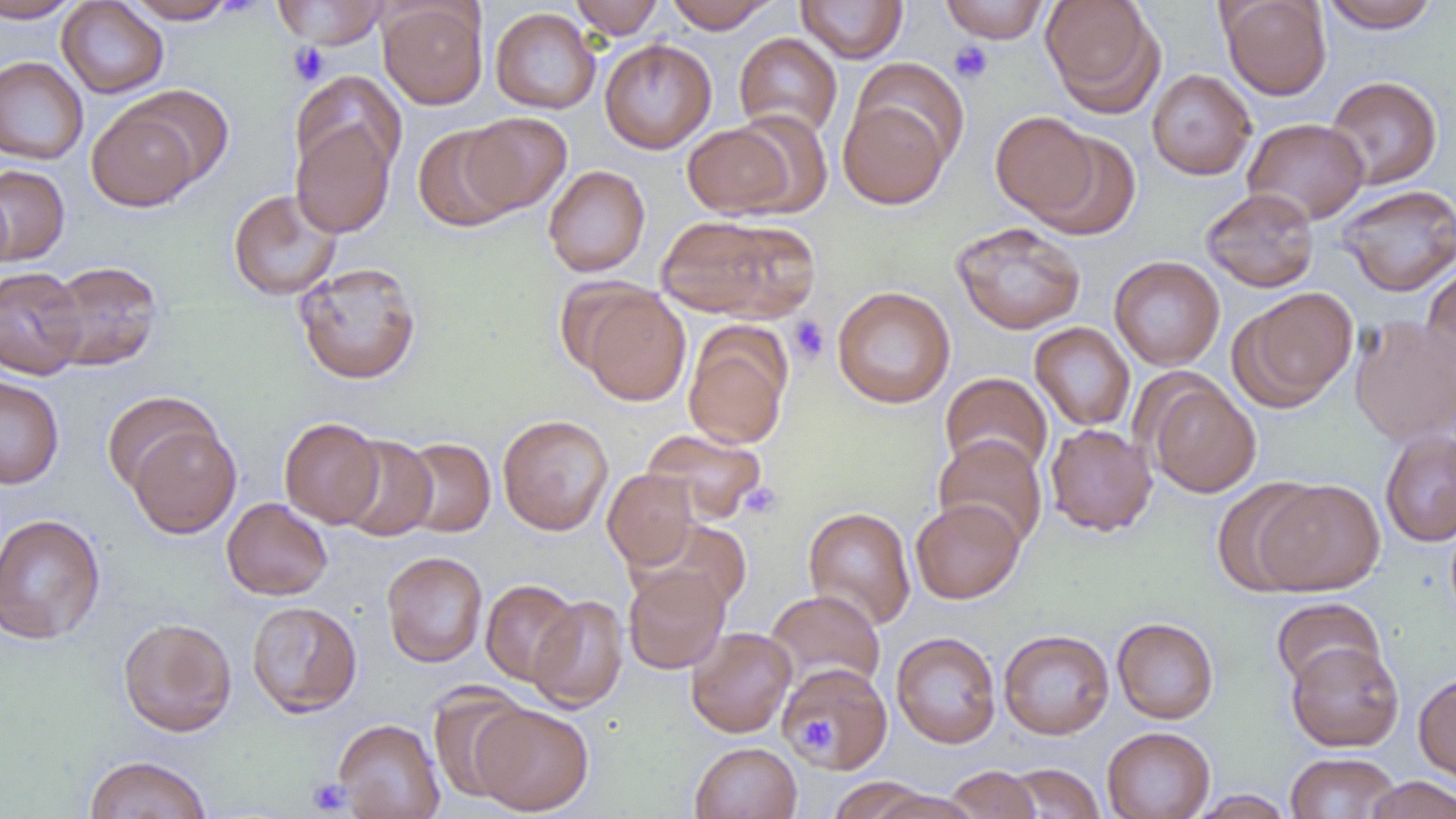

Summary:
  - Coordinate format: approximate bounding boxes as (x1,y1)-(x2,y2) corner pairs in pixels
  - Platelet locations: (948,41)-(993,84), (287,43)-(329,85), (788,316)-(830,365), (738,482)-(783,521), (798,716)-(835,751), (306,777)-(352,815)
  - Uninfected red blood cell locations: (0,0)-(83,23), (121,0)-(238,24), (272,0)-(389,48), (569,0)-(665,38), (664,0)-(776,33), (796,0)-(908,63), (939,0)-(1050,43), (1041,0)-(1164,115), (1219,0)-(1332,100), (1319,0)-(1442,33), (57,1)-(169,99), (379,2)-(488,109), (489,7)-(600,114), (734,32)-(843,139), (599,39)-(716,154), (0,56)-(89,164), (1146,69)-(1257,180), (290,71)-(406,181), (1324,75)-(1443,189), (121,84)-(235,188), (838,95)-(953,209), (86,103)-(201,212), (727,110)-(835,216), (991,111)-(1099,222), (461,112)-(572,215), (1242,117)-(1370,224), (290,120)-(396,239), (681,121)-(802,219), (413,123)-(523,232), (1030,131)-(1140,241), (0,164)-(69,266), (544,165)-(650,276), (1337,184)-(1456,296), (1201,187)-(1320,292), (228,189)-(343,301), (655,214)-(806,319), (950,221)-(1086,335), (1109,255)-(1225,371), (44,260)-(163,371), (293,261)-(422,385), (1422,263)-(1456,384), (0,265)-(87,379), (572,284)-(691,405), (832,286)-(956,409), (1232,287)-(1358,411), (1349,315)-(1456,445), (1029,322)-(1136,432), (683,324)-(793,450), (940,372)-(1053,478), (0,375)-(65,489), (1144,377)-(1261,497), (100,391)-(220,495), (498,414)-(613,535), (279,417)-(384,527), (128,421)-(241,539), (1045,423)-(1158,536), (642,428)-(767,525), (1379,429)-(1456,546), (335,434)-(438,541), (933,434)-(1048,550), (398,437)-(495,537), (603,469)-(699,570), (1212,478)-(1323,596), (1254,478)-(1386,595), (222,497)-(333,600), (910,498)-(1024,604), (803,506)-(916,630), (0,513)-(106,646), (382,551)-(488,667), (622,565)-(730,674), (480,579)-(582,686), (765,589)-(885,693), (528,595)-(628,713), (1271,597)-(1385,692), (246,601)-(363,717), (117,617)-(237,736), (1112,617)-(1219,724), (686,626)-(796,738), (999,629)-(1114,739), (891,631)-(1002,749), (1286,640)-(1404,751), (779,663)-(894,773), (1414,672)-(1456,785), (427,685)-(533,804), (473,703)-(594,815), (333,718)-(445,819), (1101,726)-(1215,819), (690,742)-(802,818), (1285,752)-(1402,818), (84,755)-(212,819), (1005,763)-(1105,818), (943,765)-(1041,819), (827,776)-(933,819), (1363,776)-(1456,819), (870,788)-(982,819), (1189,789)-(1295,818)
  - Slide-level diagnosis: negative for blood parasites
  - Image size: 1456×819 pixels
  - Modality: light microscopy
  - Magnification: 1000x
  - Field of view: single
  - Preparation: thin blood smear